Report the malaria status of this cell.
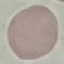

It is uninfected.

preparation = thin blood smear
capture = smartphone through the microscope eyepiece
stain = Giemsa
image type = automatically extracted cell patch, resized to 64 × 64 pixels